Assess this cell for malaria.
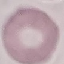
It is uninfected.

Summary:
  - Stain: Giemsa
  - Image type: cell patch, automatically extracted from a larger field of view and resized to 64 × 64 pixels
  - Capture: smartphone through the microscope eyepiece
  - Preparation: thin blood film